Mark where platelets are.
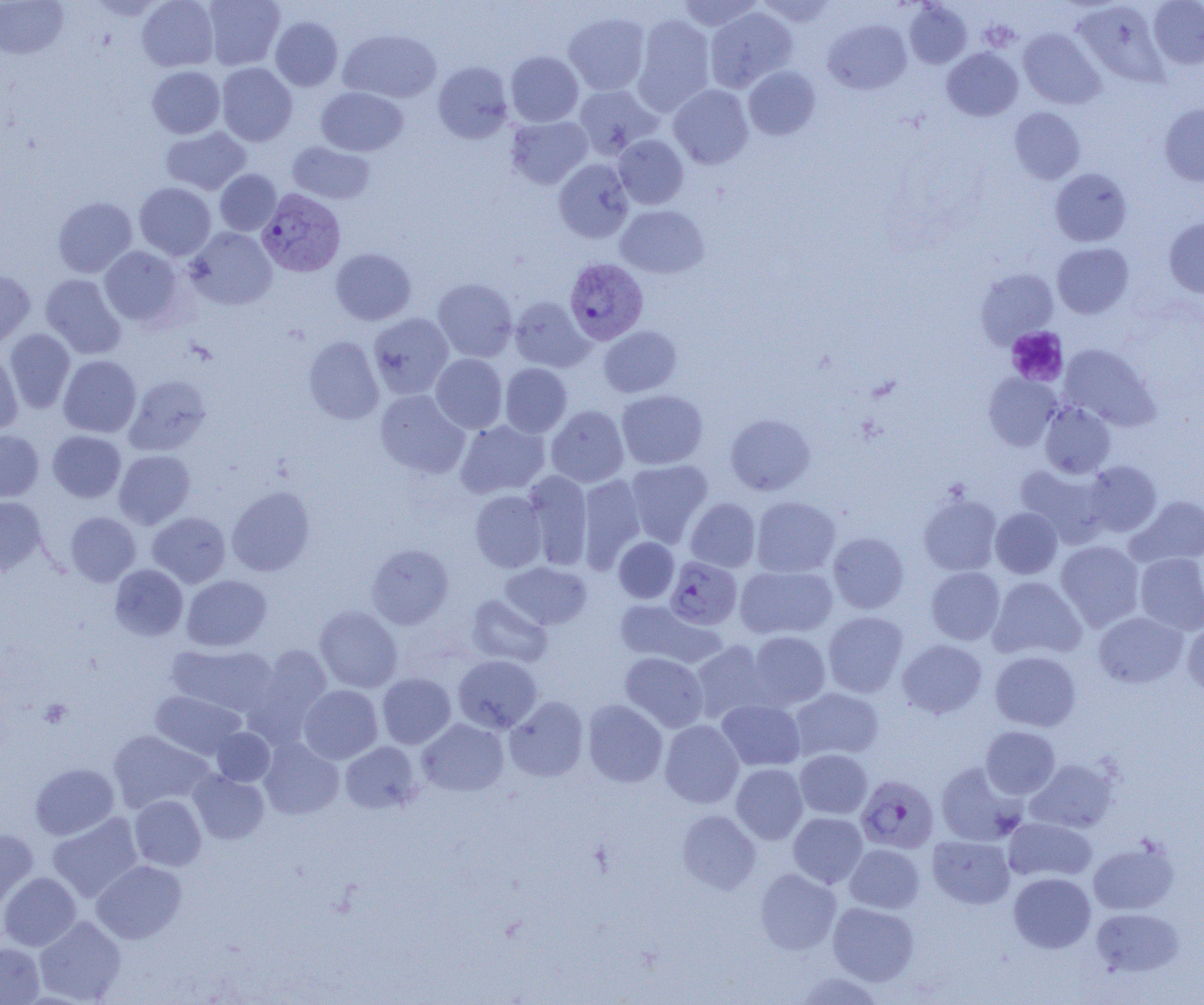
Approximate bounding boxes as (x1,y1)-(x2,y2) corner pairs in pixels.
Platelets: (1006,327)-(1068,387), (39,699)-(72,728).

Plasmodium vivax-infected red blood cell locations: (257,189)-(346,277), (564,257)-(649,344), (665,556)-(742,629), (856,775)-(938,853). Uninfected red blood cell locations: (0,0)-(68,59), (85,0)-(167,20), (137,0)-(218,71), (203,0)-(284,70), (676,0)-(764,31), (756,0)-(837,27), (1148,0)-(1204,69), (1073,1)-(1169,87), (904,2)-(972,69), (705,6)-(797,92), (563,12)-(650,95), (632,15)-(715,114), (270,17)-(343,91), (824,20)-(911,94), (1018,28)-(1105,109), (338,29)-(441,103), (942,48)-(1023,121), (506,51)-(583,126), (433,61)-(513,143), (216,63)-(297,146), (147,66)-(225,138), (743,66)-(820,140), (573,84)-(661,159), (668,84)-(753,169), (316,87)-(408,156), (1160,103)-(1204,186), (1009,106)-(1085,184), (506,115)-(592,189), (161,126)-(251,195), (614,134)-(689,209), (287,141)-(374,204), (553,158)-(634,243), (1050,168)-(1132,247), (215,169)-(281,235), (134,182)-(216,260), (53,197)-(137,277), (615,205)-(709,278), (1163,217)-(1204,298), (186,227)-(276,310), (1052,243)-(1133,318), (100,246)-(183,327), (331,248)-(416,325), (976,269)-(1058,346), (0,270)-(35,348), (40,274)-(126,359), (433,278)-(517,362), (510,296)-(593,372), (368,312)-(454,399), (599,325)-(681,397), (4,329)-(75,413), (304,336)-(383,423), (1059,344)-(1160,431), (0,351)-(23,434), (430,354)-(507,433), (58,355)-(141,437), (500,363)-(572,437), (983,373)-(1061,450), (124,375)-(211,455), (616,389)-(708,469), (375,390)-(469,478), (1040,402)-(1116,478), (546,405)-(629,487), (725,413)-(815,495), (456,419)-(550,498), (0,430)-(43,501), (48,431)-(126,502), (114,449)-(195,528), (625,459)-(713,547), (1083,460)-(1162,536), (1016,463)-(1110,547), (522,471)-(592,569), (578,474)-(646,572), (227,486)-(315,576), (470,490)-(547,573), (918,492)-(1002,576), (1126,495)-(1204,567), (0,496)-(45,575), (751,496)-(840,577), (685,498)-(760,572), (990,507)-(1062,579), (66,512)-(141,586), (147,512)-(230,587), (828,532)-(909,613), (613,537)-(679,603), (1056,540)-(1145,631), (366,543)-(453,629), (1134,553)-(1204,635), (501,561)-(591,629), (109,564)-(188,641), (735,565)-(838,639), (926,566)-(1005,645), (181,575)-(272,651), (988,576)-(1086,661), (467,595)-(552,667), (614,599)-(724,669), (314,605)-(403,692), (823,611)-(908,697), (1093,611)-(1188,688), (1182,617)-(1204,697), (747,631)-(831,709), (898,639)-(987,719), (690,640)-(772,723), (167,644)-(277,716), (245,645)-(333,743), (989,651)-(1081,731), (620,652)-(709,732), (453,655)-(542,733), (377,673)-(455,748), (299,684)-(382,764), (790,687)-(884,762), (150,691)-(245,759), (504,696)-(588,782), (582,699)-(667,788), (716,699)-(805,771), (417,718)-(509,796), (659,720)-(744,808), (981,725)-(1060,798), (212,727)-(275,786), (109,730)-(214,813), (259,738)-(344,820), (340,741)-(422,813), (795,749)-(872,819), (1025,759)-(1117,833), (935,761)-(1027,846), (30,763)-(119,840), (731,763)-(808,844), (188,770)-(269,844), (130,795)-(206,871), (677,810)-(761,894), (47,812)-(143,902), (788,812)-(867,887), (1003,817)-(1097,883), (0,828)-(38,912), (927,835)-(1014,909), (1087,837)-(1180,915), (845,843)-(925,913), (92,860)-(186,943), (755,868)-(841,954), (0,872)-(81,951), (1008,872)-(1095,953), (828,902)-(919,985), (1091,907)-(1183,977), (34,916)-(126,1004), (0,943)-(44,1004), (792,970)-(886,1004). Slide-level diagnosis: Plasmodium vivax. Single field of view. Thin blood smear. Image is 1204×1005 pixels. Captured at 1000x magnification. Light microscopy.